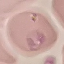
Result: negative for malaria parasites. Thin blood film. Cell patch, automatically extracted from a larger field of view and resized to 64 × 64 pixels. Giemsa-stained preparation. Photographed with a smartphone camera at the microscope eyepiece.